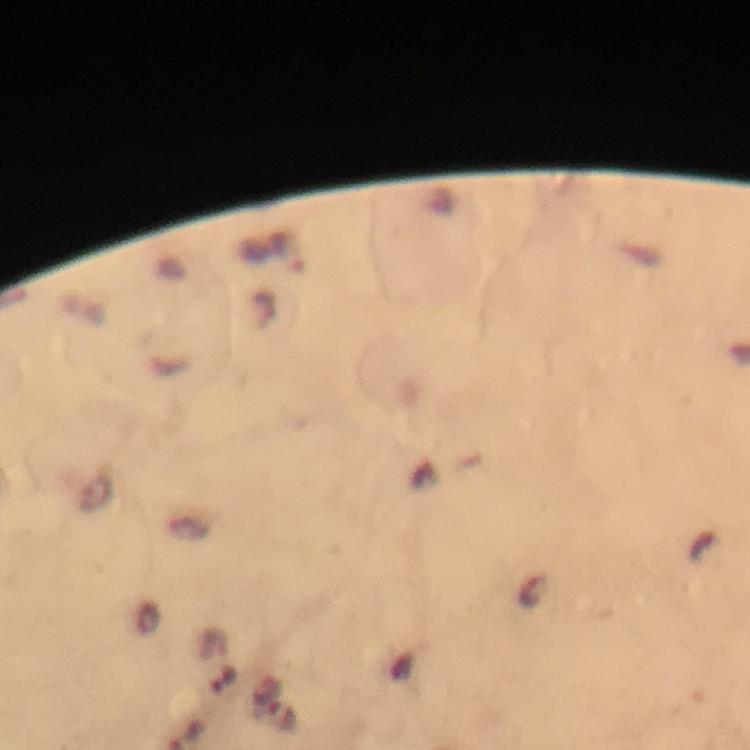

{
  "stain": "Giemsa",
  "preparation": "thick smear",
  "magnification": "100x",
  "immersion_oil": "applied",
  "context": "from a malaria diagnostic workup",
  "capture": "smartphone camera through the microscope",
  "cropped_from": "one field of view",
  "image_size": "750×750 pixels",
  "malaria_parasite_locations": "approximate centers as [x, y] in pixels: [283, 718]"
}